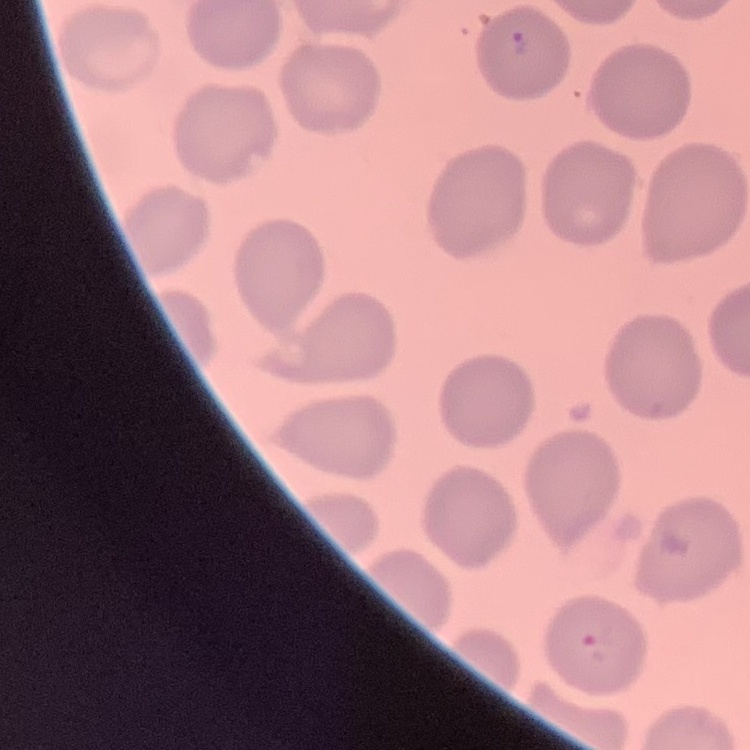

Summary:
  - Red blood cell morphology: no rouleaux formation
  - Image type: square crop of a larger photomicrograph
  - Stain: Field's or Giemsa
  - Preparation: thin blood film